Classify this cell by malaria status.
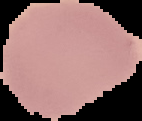
Uninfected.

Image is 142×121 pixels. From a thin blood film. Cell region segmented out of the field of view; the surrounding area is masked to black.